Report the malaria status of this cell.
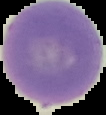

Uninfected.

image type = cell region segmented out of the field of view; surrounding area masked to black
image size = 106×115 pixels
preparation = thin blood film